Assess the morphology of the erythrocytes.
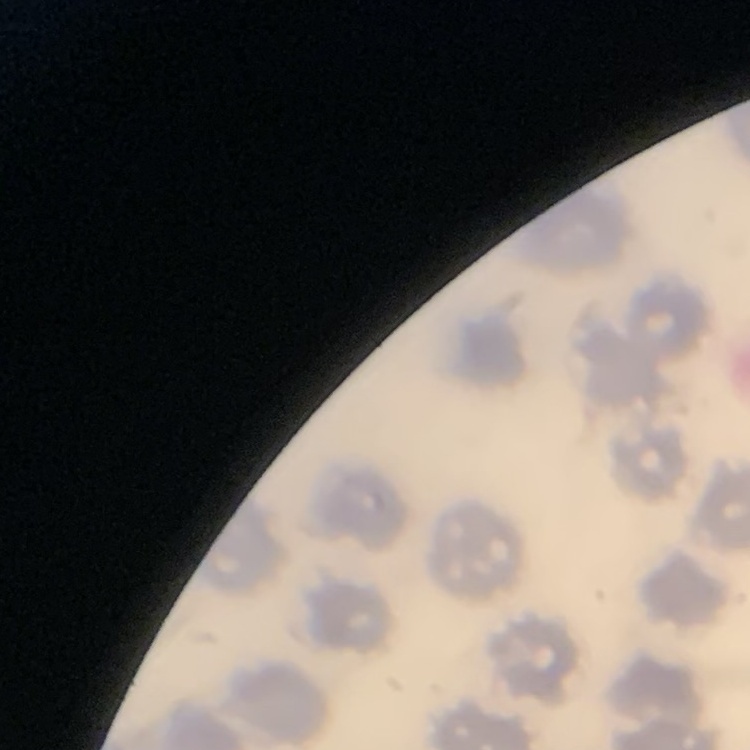
No rouleaux formation.

preparation: thin blood film
stain: Field's or Giemsa
image_type: one tile cut from a larger photomicrograph